Point out each malaria parasite and classify it by life-cycle stage.
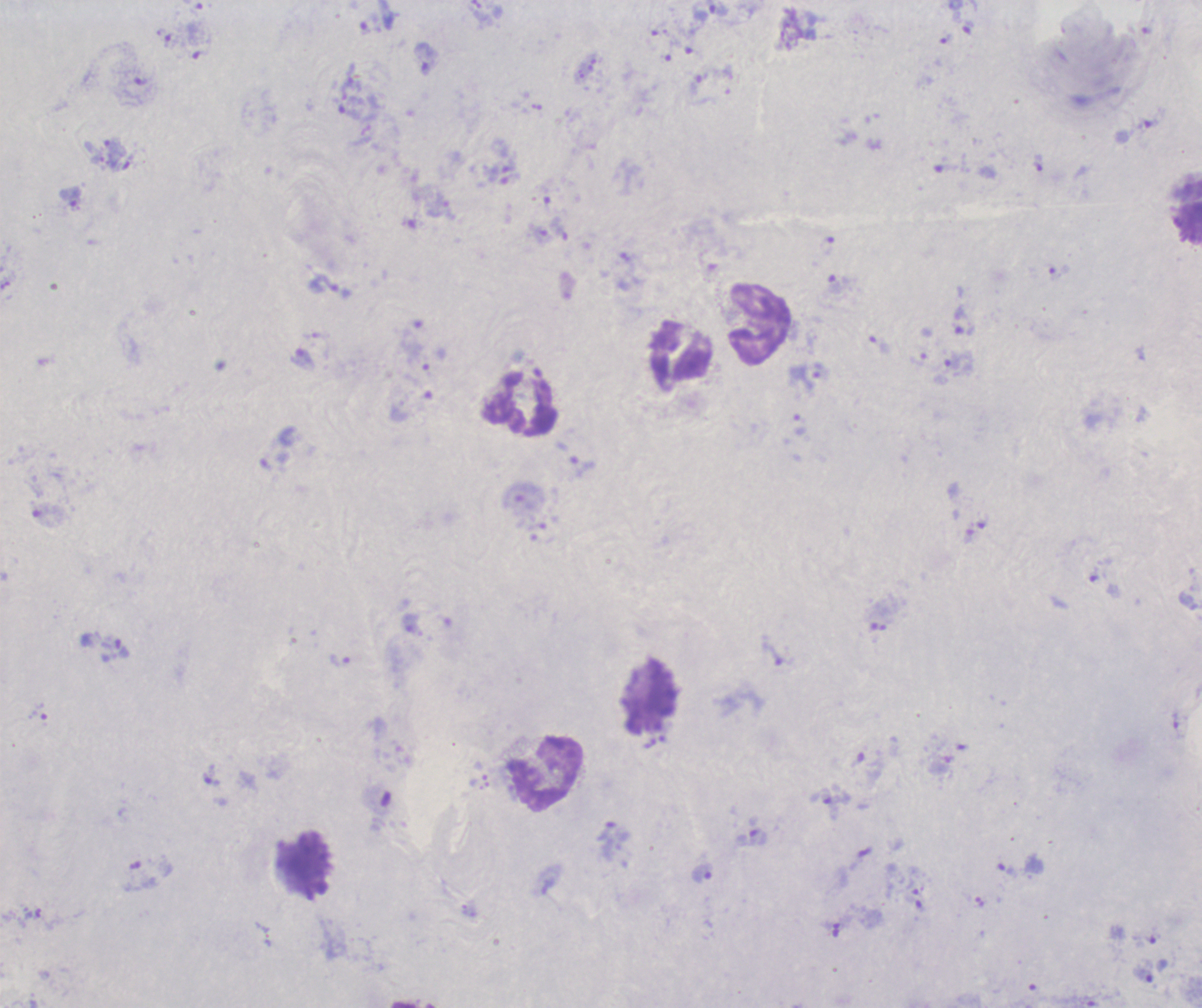
Approximate object centers, in pixels from the top-left corner.
Trophozoites: (x=710, y=10), (x=427, y=59), (x=350, y=111), (x=114, y=152), (x=70, y=199), (x=963, y=321), (x=303, y=359), (x=953, y=362), (x=809, y=376), (x=581, y=466), (x=115, y=649), (x=340, y=661), (x=211, y=776), (x=830, y=803), (x=757, y=837), (x=1007, y=870), (x=702, y=873), (x=1144, y=973).
No schizont or gametocyte forms observed.

coordinate format = approximate object centers, in pixels from the top-left corner
leukocyte locations = (x=758, y=324), (x=680, y=357), (x=521, y=405), (x=649, y=699), (x=546, y=773), (x=305, y=866)
stain = Romanowsky
preparation = thick blood smear
background quality = poor
magnification = 100x
image size = 1202×1008 pixels
field of view = one from this slide
context = previously used in a real diagnosis